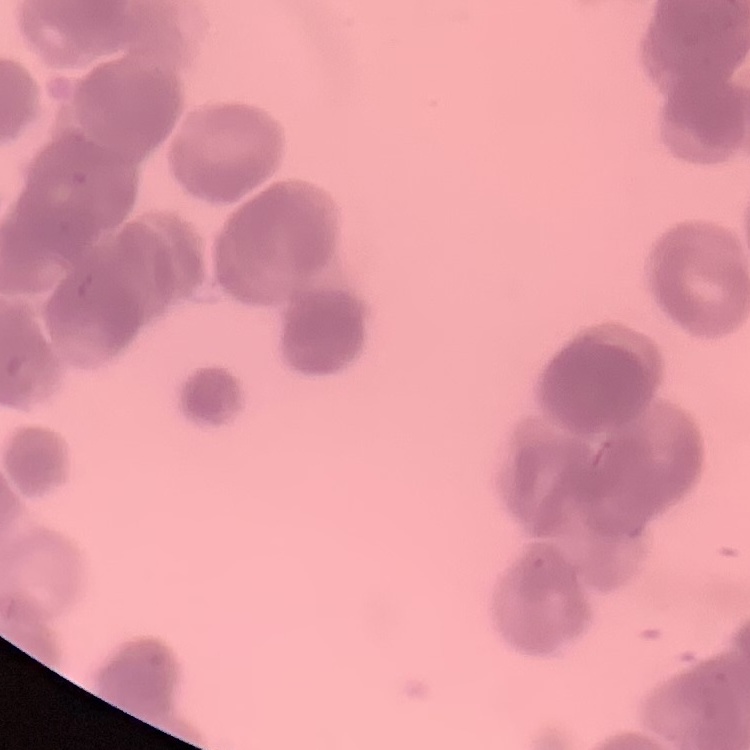

erythrocyte morphology = rouleaux formation
image type = one tile cut from a larger photomicrograph
stain = Field's or Giemsa
preparation = thin blood smear